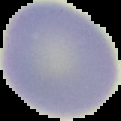
Result: negative for Plasmodium parasites. Image is 121×121 pixels. Segmented cell region on a black background. From a thin blood film.